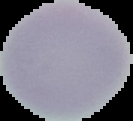
{
  "image_type": "segmented cell region with the area outside set to black",
  "result": "no malaria parasites seen",
  "image_size": "133×121 pixels",
  "preparation": "thin blood smear"
}